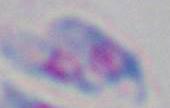
Photomicrograph. Captured at 1000x magnification. Toxoplasma gondii is seen.